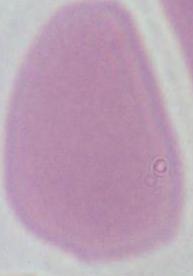
A red blood cell is shown. Photomicrograph. 1000x magnification.